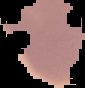

image_size: 85×88 pixels
malaria_status: uninfected
preparation: thin blood film
image_type: segmented cell region on a black background